Assess this cell for malaria.
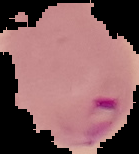

It is parasitized.

Summary:
  - Image size: 139×154 pixels
  - Preparation: thin blood smear
  - Image type: segmented cell region on a black background